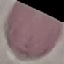 Result: no malaria parasites seen. Giemsa stain. Cell patch, automatically extracted from a larger field of view and resized to 64 × 64 pixels. Thin smear of blood. Acquired by smartphone through the microscope eyepiece.